Give the position of every malaria parasite and every leukocyte.
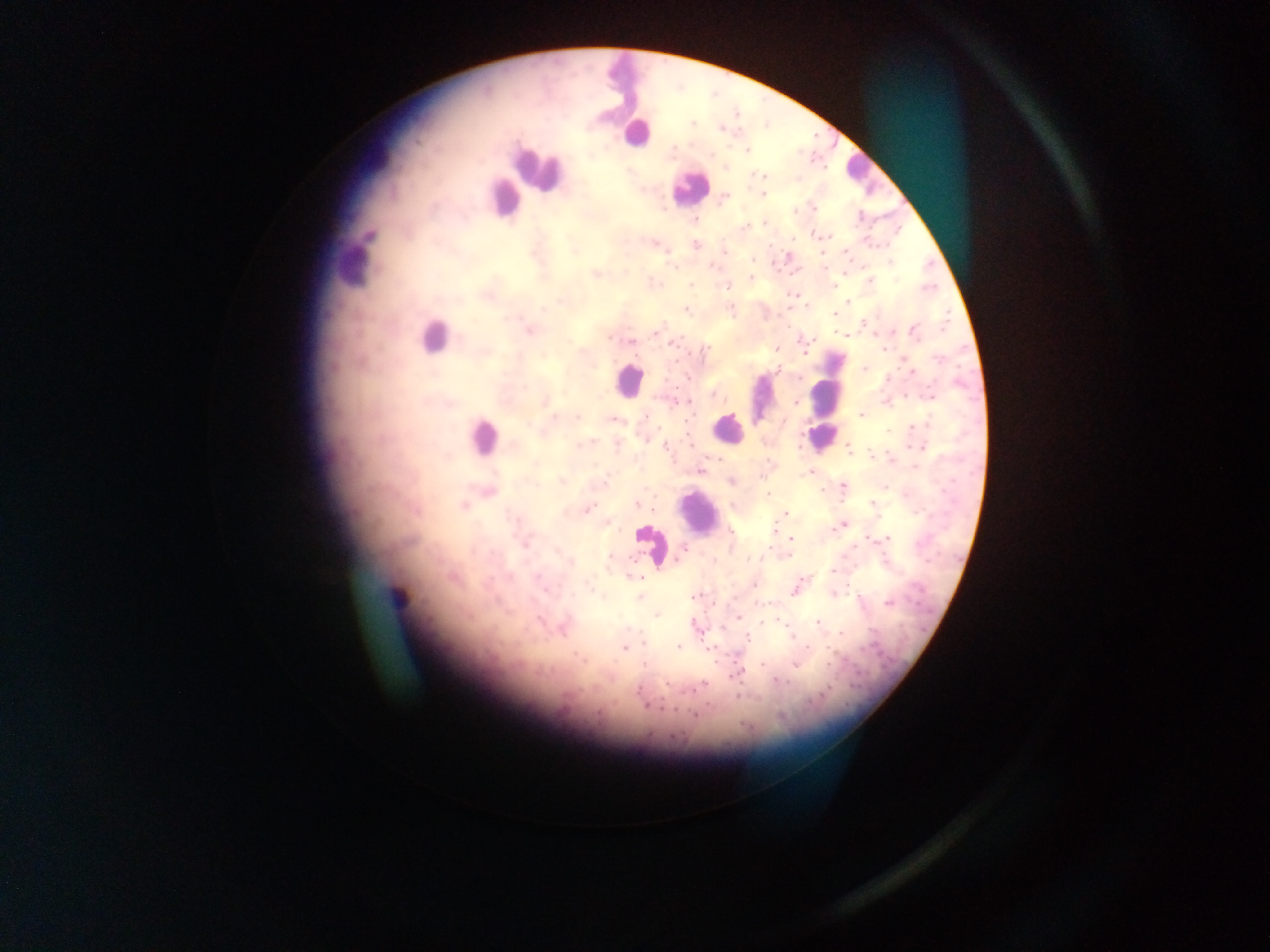

Approximate centers as (x, y) in pixels.
Malaria parasites: (692, 124), (720, 128), (747, 150), (712, 154), (591, 156), (725, 169), (755, 174), (764, 175), (759, 176), (763, 194), (725, 196), (813, 208), (695, 220), (765, 223), (745, 228), (826, 236), (793, 240), (653, 244), (768, 245), (695, 246), (575, 252), (724, 252), (822, 252), (845, 252), (752, 260), (889, 262), (672, 267), (713, 267), (596, 274), (751, 277), (870, 281), (652, 282), (691, 285), (726, 287), (832, 287), (792, 294), (561, 301), (849, 301), (543, 309), (686, 309), (732, 311), (835, 315), (864, 322), (530, 332), (656, 332), (914, 332), (844, 335), (610, 338), (631, 341), (674, 343), (775, 349), (883, 350), (705, 352), (805, 353), (940, 359), (864, 369), (777, 370), (912, 372), (688, 378), (799, 379), (664, 380), (712, 395), (932, 396), (719, 397), (676, 401), (544, 402), (685, 402), (796, 402), (886, 403), (578, 418), (614, 419), (783, 421), (915, 427), (888, 431), (645, 439), (588, 443), (582, 444), (689, 444), (617, 445), (666, 447), (922, 447), (848, 448), (870, 455), (716, 458), (891, 459), (701, 470), (811, 472), (760, 478), (562, 481), (732, 481), (604, 482), (843, 486), (885, 486), (821, 490), (645, 491), (767, 495), (872, 503), (637, 505), (464, 506), (587, 509), (654, 510), (785, 514), (607, 523), (844, 524), (839, 526), (774, 529), (731, 532), (791, 537), (868, 538), (887, 539), (854, 549), (684, 550), (788, 555), (611, 556), (678, 558), (758, 558), (714, 562), (833, 570), (640, 578), (754, 585), (589, 586), (794, 591), (833, 594), (693, 596), (640, 597), (889, 603), (656, 615), (739, 617), (539, 620), (818, 622), (722, 629), (840, 633), (790, 636), (747, 639), (643, 643), (807, 646), (677, 647), (625, 648), (761, 665), (795, 665), (775, 681), (703, 683), (666, 685), (698, 687), (695, 689), (638, 690), (738, 697), (644, 706), (662, 708), (694, 715), (672, 736).
Leukocytes: (621, 83), (637, 133), (380, 153), (860, 168), (536, 171), (687, 187), (504, 198), (353, 265), (434, 340), (627, 381), (829, 382), (761, 396), (727, 429), (482, 436), (820, 439), (699, 513), (645, 549), (398, 596).

Summary:
  - Field of view: single
  - Preparation: thick blood film
  - Capture: mobile-phone photograph through a microscope
  - Image size: 1270×952 pixels
  - Country: Ghana